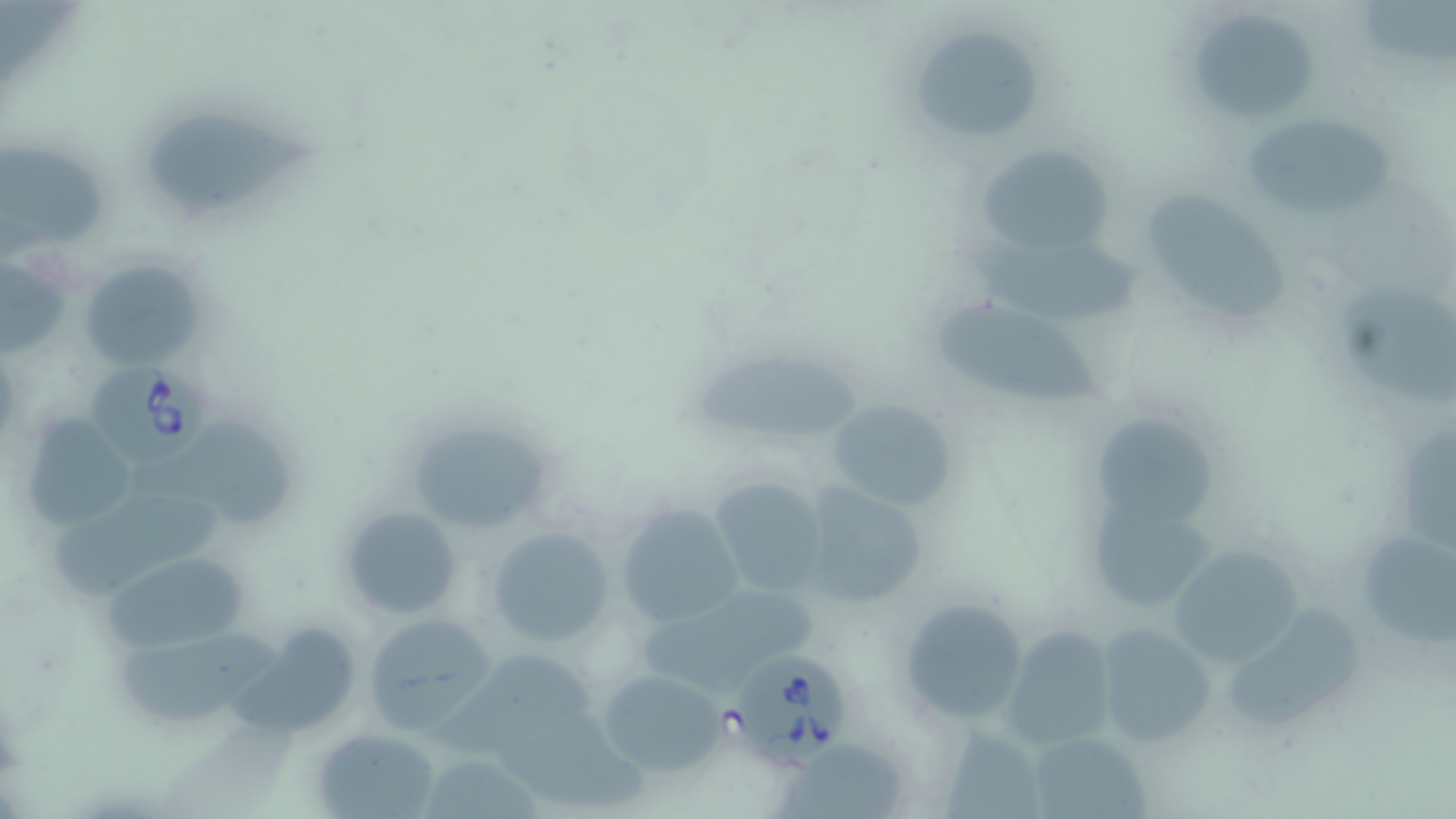

Summary:
  - Coordinate format: approximate bounding boxes as (x1,y1)-(x2,y2) corner pairs in pixels
  - Uninfected red blood cell locations: (1363,1)-(1453,68), (1197,13)-(1322,125), (906,22)-(1050,151), (149,103)-(323,210), (1247,111)-(1393,219), (0,138)-(114,259), (974,144)-(1113,254), (1150,193)-(1291,323), (968,238)-(1141,322), (77,257)-(203,370), (1338,290)-(1455,405), (937,299)-(1103,403), (686,355)-(862,442), (826,396)-(958,515), (19,414)-(142,528), (402,414)-(561,536), (1098,418)-(1216,534), (141,423)-(302,527), (1400,432)-(1456,554), (709,475)-(831,596), (797,482)-(927,610), (47,485)-(235,597), (1089,497)-(1217,610), (615,502)-(743,626), (337,504)-(462,619), (1363,525)-(1456,650), (484,526)-(617,648), (1167,544)-(1303,668), (103,551)-(250,653), (634,586)-(819,694), (897,598)-(1030,723), (1224,605)-(1363,732), (361,612)-(493,733), (1094,623)-(1214,748), (117,625)-(283,727), (1003,626)-(1119,746), (228,627)-(355,735), (422,649)-(602,760), (596,668)-(727,776), (504,718)-(656,815), (944,727)-(1043,819), (313,728)-(442,818), (1026,729)-(1149,819), (782,740)-(909,819), (419,755)-(545,817)
  - Babesia divergens-infected red blood cell locations: (88,359)-(211,469), (732,655)-(845,764)
  - Slide-level diagnosis: Babesia divergens
  - Magnification: 1000x
  - Stain: May-Grünwald-Giemsa
  - Modality: optical microscopy
  - Preparation: thin blood film
  - Image size: 1456×819 pixels
  - Field of view: single